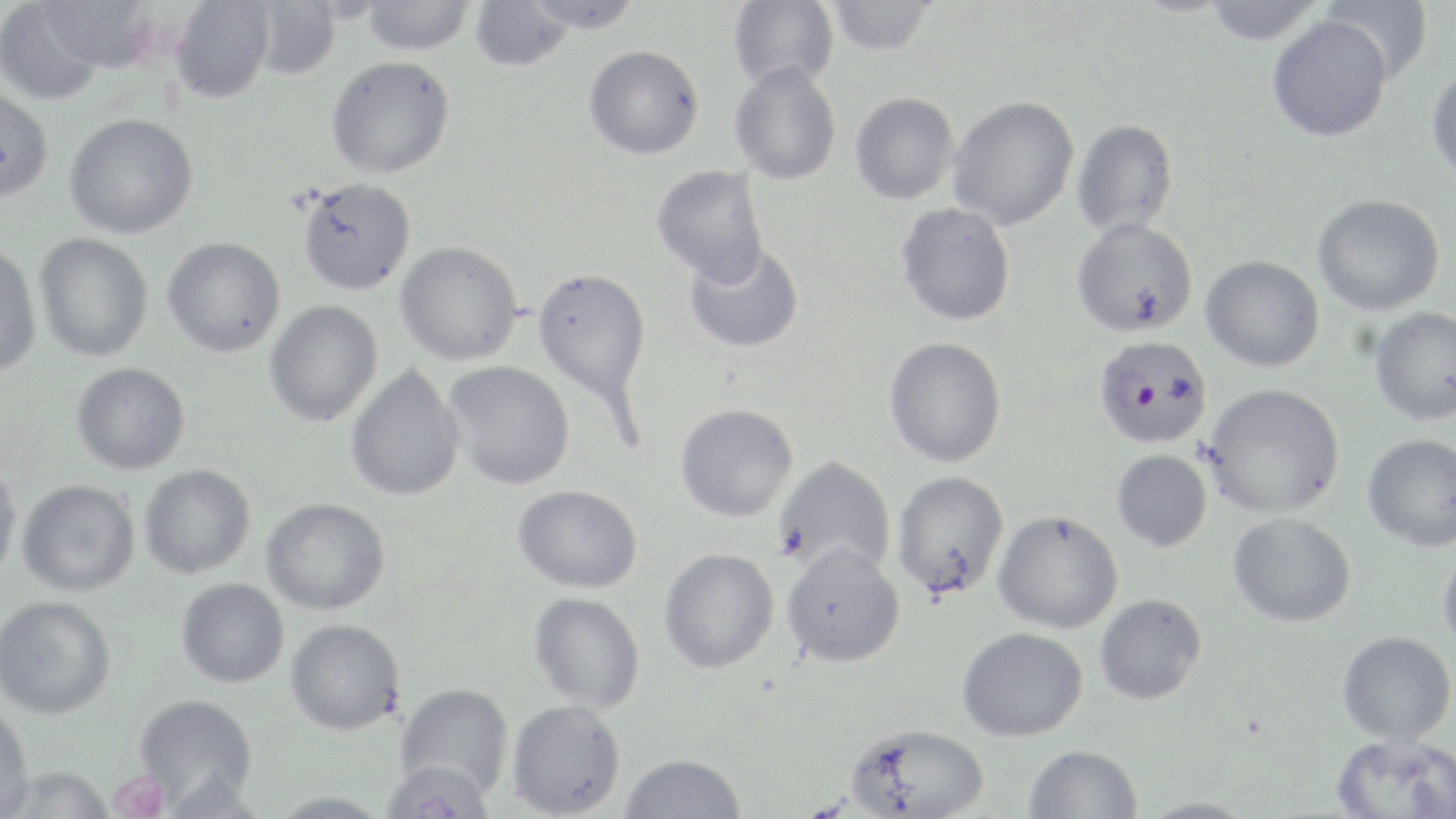
plasmodium_falciparum_infected_red_blood_cell_locations: 'approximate bounding boxes as (x1, y1, x2, y2) in pixels: (1092, 335, 1212, 448)'
slide_level_diagnosis: Plasmodium falciparum
stain: May-Grünwald-Giemsa
image_size: 1456×819 pixels
magnification: 1000x
modality: light microscopy
uninfected_red_blood_cell_locations: 'approximate bounding boxes as (x1, y1, x2, y2) in pixels: (360, 0, 475, 56), (469, 0, 574, 71), (521, 0, 644, 33), (728, 0, 839, 92), (1320, 0, 1434, 83), (0, 1, 109, 105), (35, 1, 158, 76), (170, 1, 275, 104), (249, 1, 342, 79), (825, 1, 936, 55), (1201, 1, 1324, 45), (1266, 15, 1393, 142), (583, 45, 704, 160), (325, 56, 456, 179), (729, 62, 841, 186), (1426, 63, 1456, 187), (0, 86, 54, 204), (850, 92, 960, 204), (948, 96, 1080, 231), (64, 113, 198, 239), (1071, 118, 1179, 238), (651, 165, 769, 285), (297, 177, 416, 295), (1312, 194, 1445, 316), (896, 203, 1016, 327), (1071, 217, 1199, 337), (34, 234, 153, 362), (162, 237, 286, 358), (394, 241, 523, 366), (0, 243, 41, 378), (683, 243, 804, 354), (1200, 255, 1325, 372), (532, 267, 651, 408), (264, 300, 383, 427), (1368, 307, 1456, 427), (884, 336, 1007, 467), (443, 360, 575, 490), (71, 362, 190, 475), (345, 365, 465, 501), (1203, 382, 1346, 519), (675, 403, 798, 522), (1361, 433, 1456, 552), (1111, 449, 1212, 551), (772, 455, 897, 578), (0, 464, 22, 582), (139, 464, 255, 579), (891, 470, 1010, 600), (17, 480, 140, 597), (513, 484, 642, 593), (261, 497, 390, 615), (992, 509, 1124, 634), (1228, 512, 1356, 627), (780, 543, 906, 667), (658, 547, 779, 674), (1438, 547, 1456, 655), (175, 578, 289, 688), (528, 592, 645, 713), (1094, 593, 1207, 705), (0, 595, 116, 720), (285, 619, 405, 736), (957, 626, 1088, 742), (1336, 631, 1455, 745), (395, 682, 514, 799), (133, 694, 259, 810), (506, 699, 626, 818), (0, 703, 35, 819), (845, 723, 989, 818), (1332, 733, 1456, 819), (1024, 744, 1142, 819), (619, 753, 747, 818), (379, 760, 496, 819), (2, 766, 115, 818), (268, 791, 391, 819), (1135, 796, 1259, 818)'
preparation: thin blood film
field_of_view: single
platelet_locations: 'approximate bounding boxes as (x1, y1, x2, y2) in pixels: (108, 770, 171, 819)'